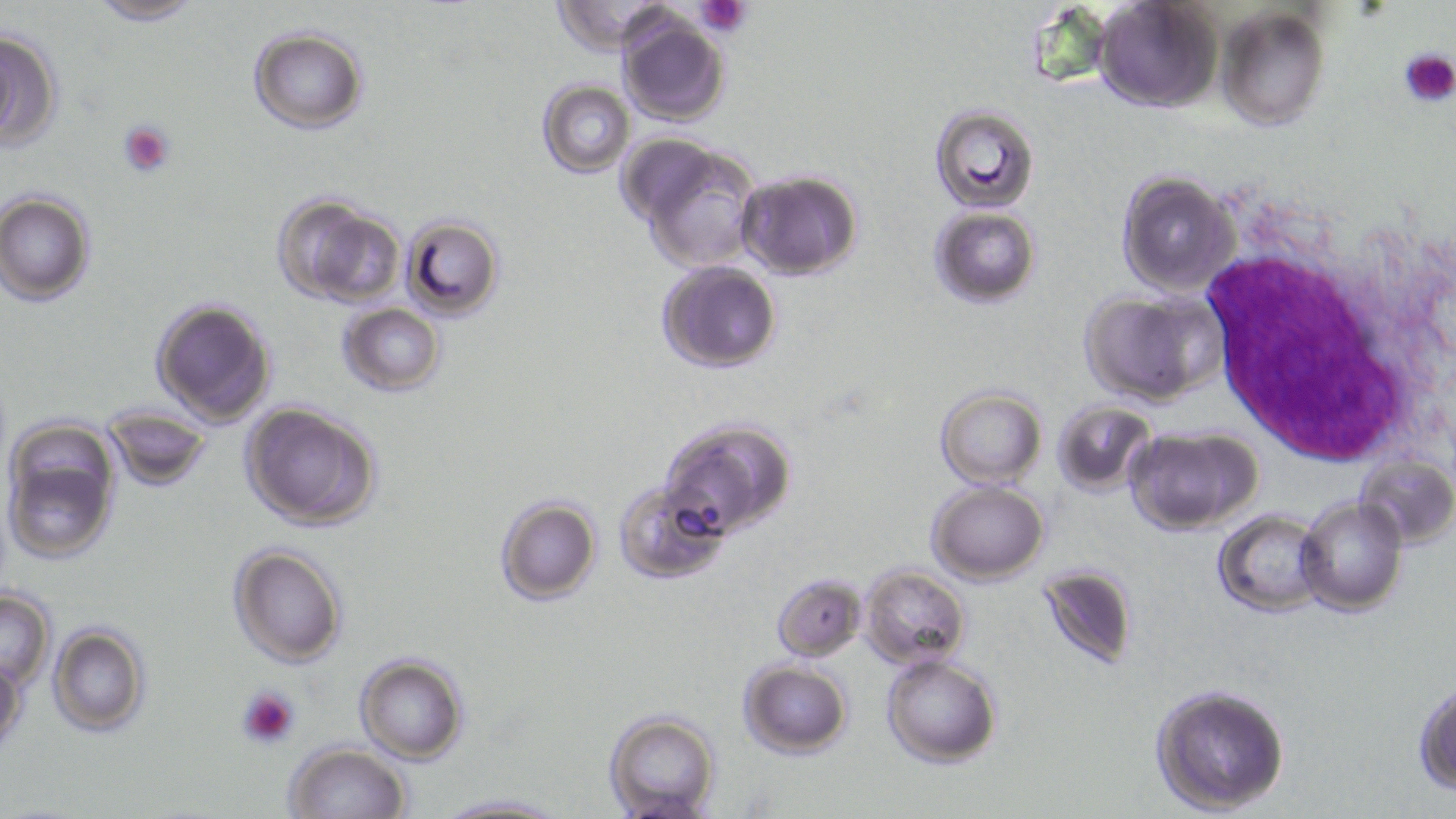 Approximate bounding boxes as [x1, y1, x2, y2] in pixels. Uninfected red blood cell locations: [81, 0, 206, 24], [551, 1, 677, 53], [1092, 1, 1223, 113], [1214, 5, 1330, 133], [614, 12, 732, 126], [0, 27, 65, 153], [247, 27, 371, 133], [537, 79, 635, 178], [930, 105, 1041, 215], [624, 135, 767, 274], [735, 169, 865, 279], [1116, 169, 1240, 297], [1, 190, 97, 305], [272, 193, 404, 308], [929, 206, 1041, 309], [400, 214, 505, 318], [655, 260, 784, 373], [1078, 287, 1228, 404], [150, 297, 278, 426], [337, 303, 447, 396], [934, 385, 1049, 489], [239, 401, 384, 532], [1051, 401, 1158, 494], [97, 405, 214, 493], [658, 416, 796, 539], [1, 418, 123, 565], [1124, 425, 1262, 534], [1360, 453, 1455, 550], [614, 479, 728, 582], [927, 479, 1050, 584], [495, 496, 602, 606], [1297, 497, 1407, 616], [1214, 509, 1330, 617], [227, 543, 346, 668], [1035, 563, 1141, 673], [859, 565, 972, 669], [772, 572, 867, 661], [0, 586, 56, 688], [47, 621, 152, 738], [0, 652, 26, 759], [354, 653, 470, 764], [880, 653, 1003, 768], [736, 659, 854, 758], [1413, 679, 1456, 794], [1149, 682, 1290, 815], [602, 711, 723, 819], [283, 744, 411, 819], [431, 793, 571, 818]. White blood cell locations: [1186, 217, 1446, 470]. Platelet locations: [697, 0, 752, 36], [1400, 47, 1455, 108], [117, 120, 174, 179], [235, 685, 300, 749]. Slide-level diagnosis: Plasmodium falciparum. One field of a larger specimen. May-Grünwald-Giemsa stain. Light microscopy. Thin blood film. Captured at 1000x magnification. Image is 1456×819 pixels.